Assess this cell for malaria.
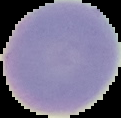

Uninfected.

preparation: thin blood smear
image_size: 121×118 pixels
image_type: segmented cell region on a black background